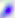
Summary:
  - Magnification: 400x
  - Modality: photomicrograph
  - Identification: Toxoplasma gondii